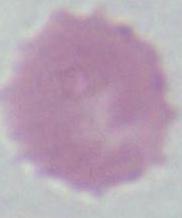 Micrograph. 1000x magnification. A red blood cell is seen.